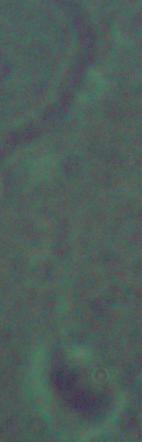
Summary:
  - Identification: Leishmania
  - Modality: photomicrograph
  - Magnification: 1000x